Assess the morphology of the erythrocytes.
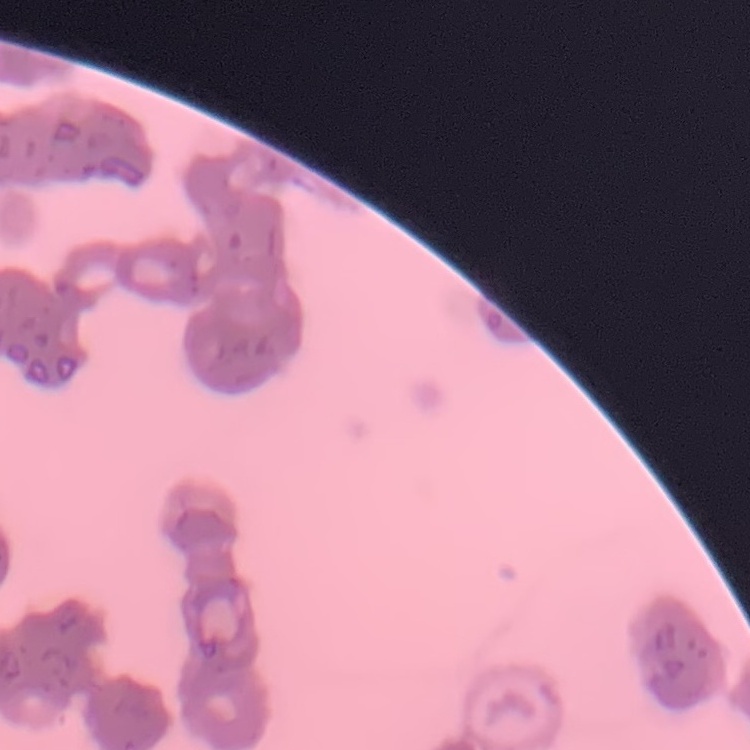

Rouleaux formation.

preparation: thin blood smear
stain: Field's or Giemsa
image_type: square crop of a larger photomicrograph